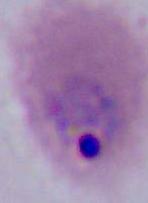

Summary:
  - Identification: Plasmodium
  - Magnification: 400x or 1000x
  - Modality: micrograph